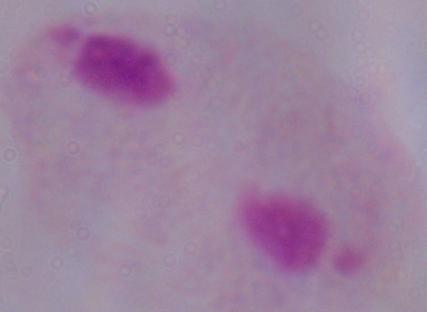

A trichomonad is shown. Photomicrograph. 1000x magnification.